Locate every Plasmodium parasite.
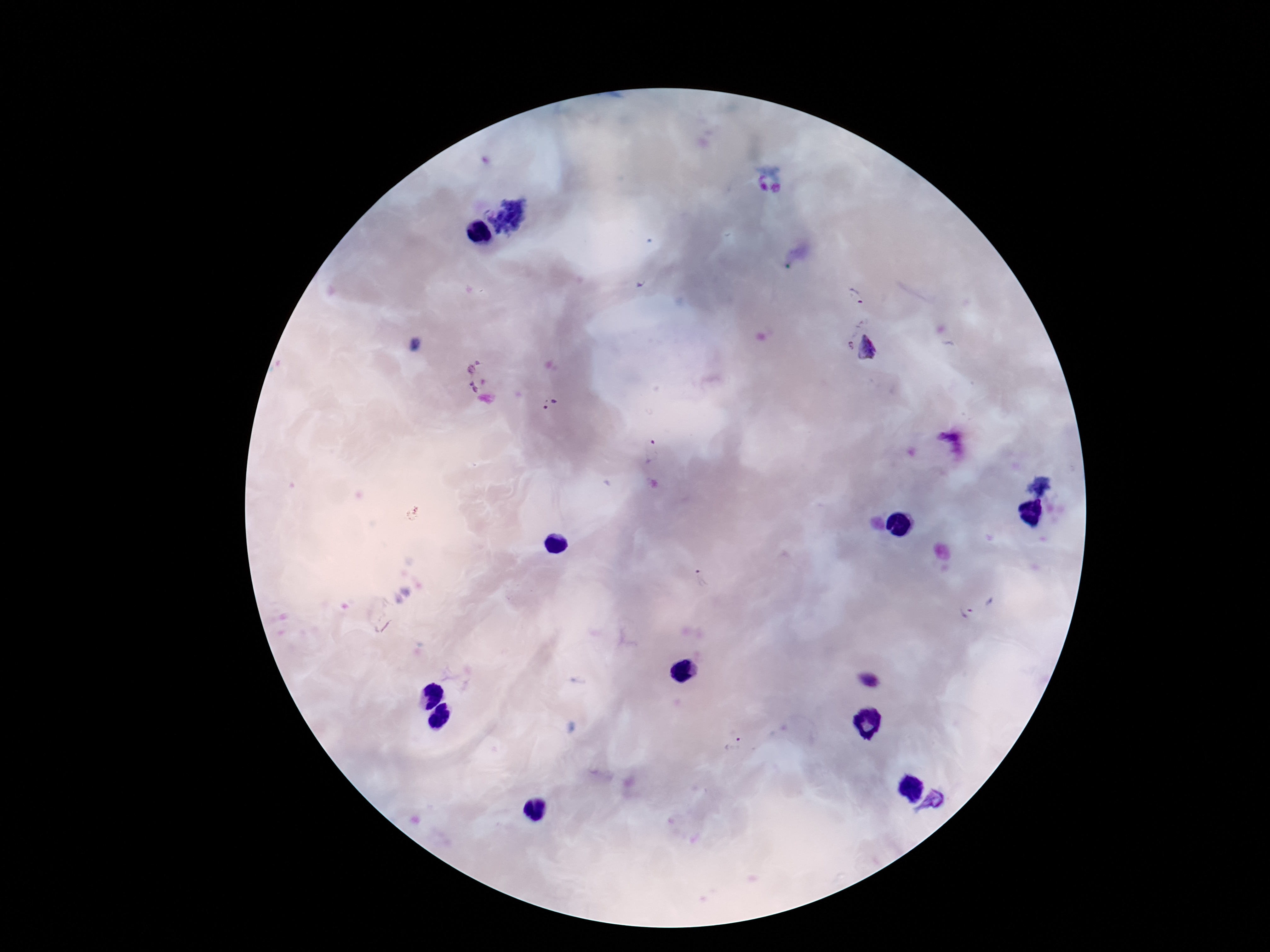

Approximate object centers, in pixels from the top-left corner.
Plasmodium parasites: (x=855, y=296), (x=849, y=346), (x=871, y=348), (x=472, y=364), (x=474, y=386), (x=550, y=404), (x=653, y=450), (x=701, y=580), (x=966, y=610), (x=735, y=744), (x=935, y=801).

Patient malaria status: infected. Thick peripheral-blood smear. One field from this slide. Smartphone photograph taken through the microscope eyepiece. Giemsa-stained preparation. 100x magnification. Image is 1270×952 pixels.